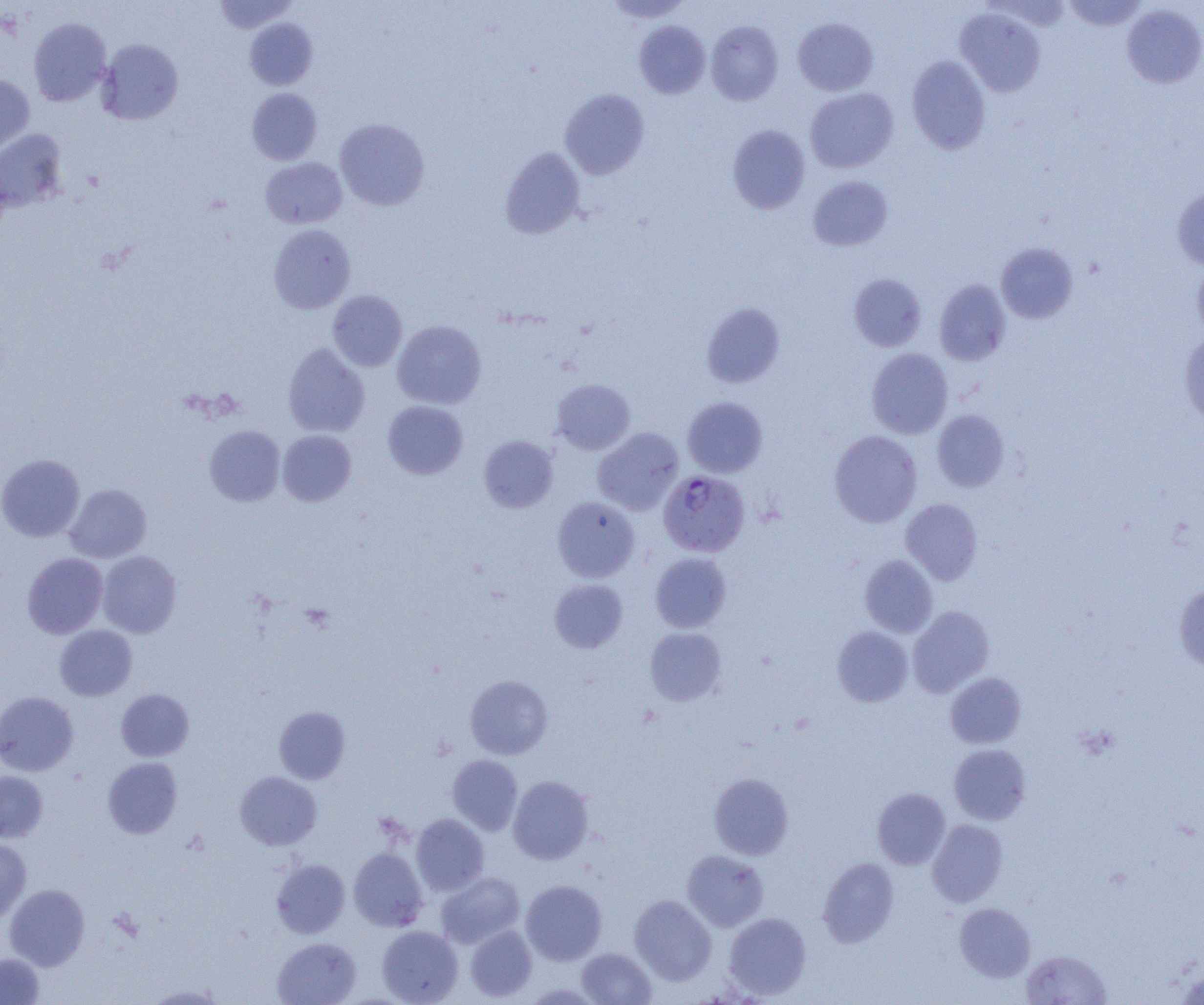

Summary:
  - Coordinate format: approximate bounding boxes as [x1, y1, x2, y2] in pixels
  - Plasmodium falciparum-infected red blood cell locations: [658, 470, 749, 557]
  - Uninfected red blood cell locations: [214, 0, 298, 33], [603, 0, 693, 22], [1062, 0, 1148, 31], [1122, 4, 1204, 88], [955, 7, 1046, 97], [28, 18, 111, 106], [244, 18, 318, 90], [793, 18, 878, 96], [634, 20, 710, 99], [706, 21, 784, 105], [97, 38, 183, 125], [906, 56, 991, 154], [0, 73, 34, 156], [247, 88, 322, 165], [805, 88, 898, 173], [560, 89, 650, 179], [335, 118, 430, 210], [727, 125, 810, 214], [0, 129, 68, 212], [500, 147, 585, 239], [261, 157, 347, 228], [808, 175, 893, 251], [1172, 186, 1204, 271], [268, 224, 356, 313], [996, 242, 1078, 324], [1192, 261, 1204, 340], [848, 273, 927, 352], [934, 279, 1011, 366], [327, 290, 407, 372], [701, 302, 785, 388], [392, 320, 486, 409], [1179, 330, 1204, 427], [283, 343, 370, 437], [866, 348, 953, 438], [552, 379, 635, 455], [682, 397, 767, 477], [382, 401, 468, 479], [932, 409, 1010, 492], [204, 425, 285, 506], [592, 427, 684, 516], [277, 430, 356, 506], [829, 430, 922, 527], [479, 435, 558, 512], [0, 454, 85, 541], [65, 484, 151, 563], [552, 496, 640, 582], [901, 498, 982, 584], [97, 551, 181, 638], [650, 552, 732, 632], [22, 553, 108, 638], [860, 555, 938, 637], [550, 579, 628, 652], [1174, 584, 1204, 672], [907, 606, 994, 697], [55, 625, 137, 701], [832, 626, 913, 706], [645, 627, 727, 705], [945, 672, 1026, 748], [465, 675, 552, 759], [116, 689, 193, 761], [0, 691, 79, 776], [273, 706, 350, 784], [949, 743, 1031, 825], [447, 755, 522, 834], [102, 757, 183, 838], [0, 770, 48, 842], [235, 771, 322, 851], [709, 773, 794, 860], [508, 775, 594, 864], [872, 787, 950, 869], [411, 814, 489, 896], [928, 819, 1008, 906], [0, 838, 31, 921], [349, 847, 428, 931], [682, 849, 768, 931], [817, 857, 899, 947], [271, 859, 350, 938], [436, 872, 524, 948], [521, 880, 607, 965], [4, 884, 89, 970], [629, 894, 716, 985], [955, 903, 1035, 981], [724, 912, 811, 999], [377, 925, 463, 1005], [465, 925, 537, 1001], [273, 937, 361, 1004], [576, 948, 656, 1005], [1020, 949, 1112, 1005], [0, 953, 44, 1005], [1174, 966, 1204, 1005], [144, 984, 227, 1004]
  - Slide-level diagnosis: Plasmodium falciparum
  - Modality: light microscopy
  - Field of view: one of a larger specimen
  - Preparation: thin blood film
  - Image size: 1204×1005 pixels
  - Magnification: 1000x